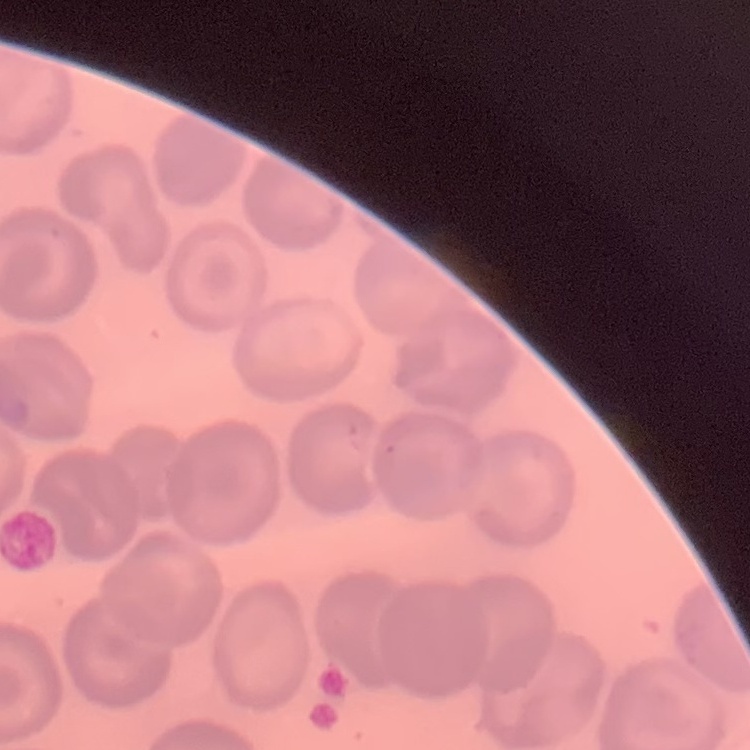

The erythrocytes show no rouleaux formation. Thin blood smear. One tile cut from a larger photomicrograph. Stained with either Field's or Giemsa.